Report the malaria status of this cell.
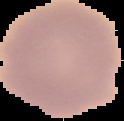

Uninfected.

Summary:
  - Preparation: thin blood film
  - Image type: cell region segmented out of the field of view; surrounding area masked to black
  - Image size: 124×121 pixels